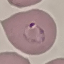
Result: malaria parasites identified. Giemsa-stained preparation. Thin smear of blood. Photographed with a smartphone camera at the microscope eyepiece. Cell patch, automatically extracted from a larger field of view and resized to 64 × 64 pixels.